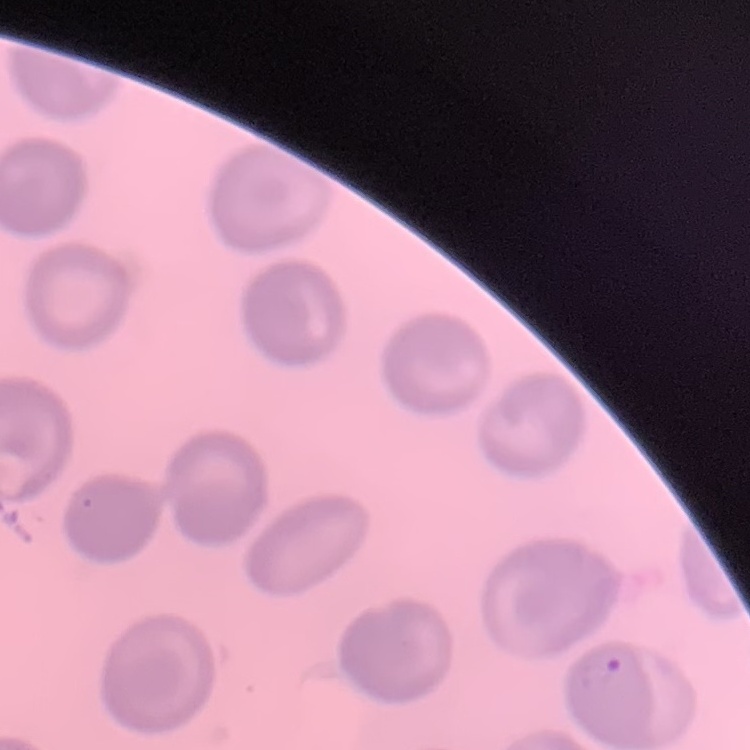
erythrocyte morphology = no rouleaux formation
image type = square crop of a larger photomicrograph
stain = Field's or Giemsa
preparation = thin peripheral smear